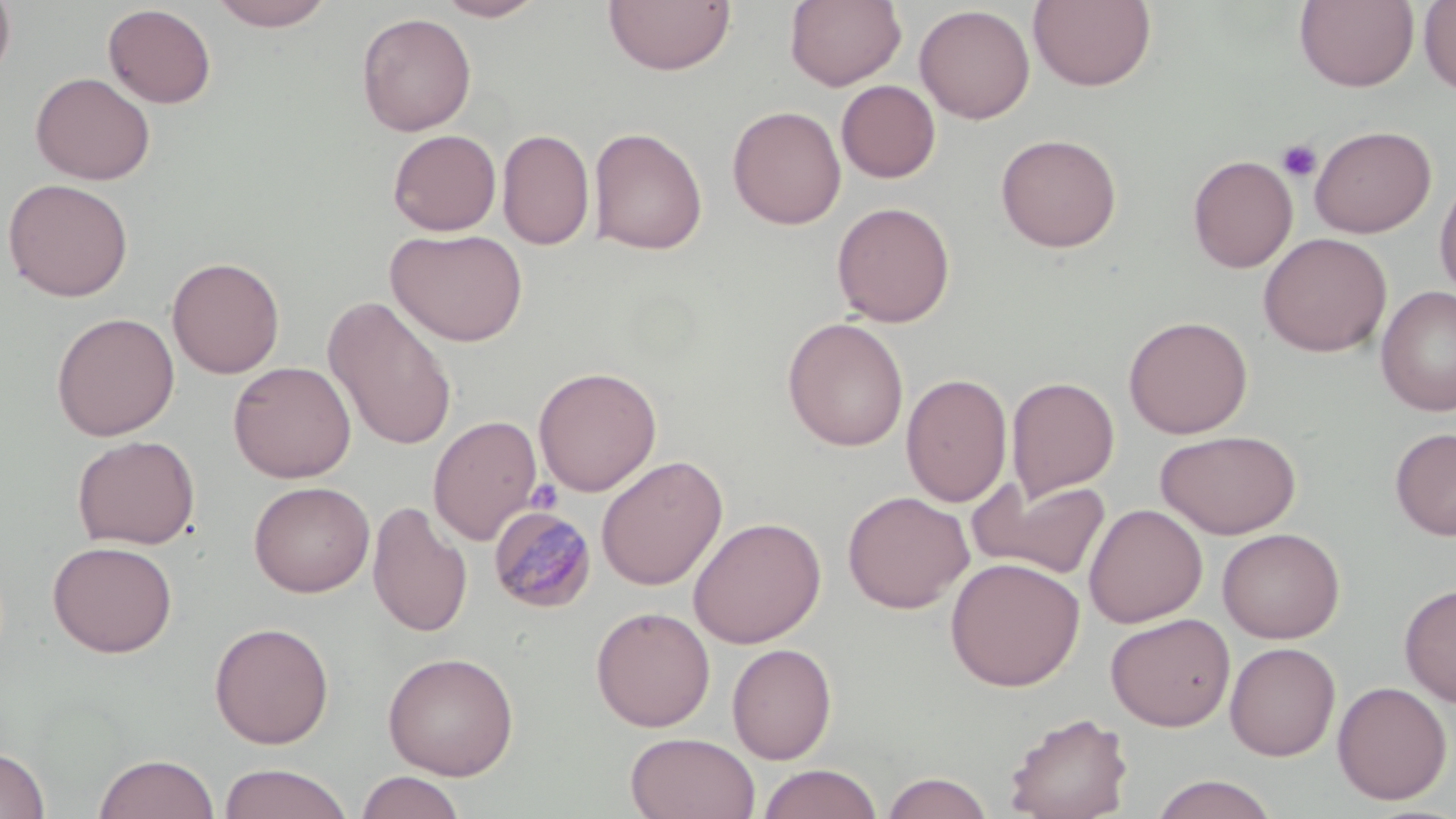 Approximate bounding boxes as (x1,y1)-(x2,y2) corner pairs in pixels. Plasmodium malariae-infected red blood cell locations: (487,504)-(597,614). Uninfected red blood cell locations: (0,0)-(16,85), (207,0)-(337,31), (434,0)-(548,21), (603,0)-(735,76), (785,0)-(906,90), (1294,0)-(1419,91), (1028,1)-(1157,91), (1419,1)-(1456,96), (102,4)-(217,108), (914,4)-(1035,124), (356,12)-(476,136), (30,71)-(156,185), (836,80)-(940,183), (728,105)-(846,230), (1309,124)-(1436,238), (588,126)-(708,255), (497,128)-(594,251), (387,129)-(501,236), (995,133)-(1122,253), (1188,154)-(1297,273), (1435,173)-(1456,302), (2,178)-(134,302), (831,201)-(955,327), (386,227)-(528,347), (1258,232)-(1392,357), (166,256)-(285,379), (1375,286)-(1456,416), (323,295)-(458,451), (50,312)-(180,440), (1123,315)-(1253,438), (782,317)-(909,451), (228,360)-(356,483), (533,366)-(662,496), (901,373)-(1013,508), (1006,376)-(1120,503), (428,415)-(543,545), (1390,427)-(1456,540), (1155,429)-(1301,539), (71,434)-(200,550), (596,455)-(728,591), (970,477)-(1111,579), (248,481)-(375,597), (841,490)-(974,614), (367,500)-(472,638), (1083,503)-(1207,628), (688,515)-(826,649), (1217,527)-(1345,643), (47,540)-(178,658), (945,557)-(1085,691), (1399,582)-(1456,707), (591,606)-(715,731), (1106,613)-(1235,731), (209,621)-(334,749), (1225,641)-(1341,761), (727,643)-(837,764), (382,651)-(519,779), (1332,680)-(1452,805), (1002,710)-(1134,819), (625,732)-(760,819), (0,746)-(51,819), (92,753)-(220,819), (217,763)-(353,819), (756,763)-(884,819), (355,770)-(467,819), (881,771)-(994,818), (1150,774)-(1279,818). Platelet locations: (1276,140)-(1322,183), (526,479)-(563,513). Slide-level diagnosis: Plasmodium malariae. Captured at 1000x magnification. One field of a larger specimen. May-Grünwald-Giemsa stain. Image is 1456×819 pixels. Thin blood film. Optical microscopy.